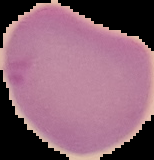
result: malaria parasites identified
preparation: thin blood film
image_type: segmented cell region on a black background
image_size: 154×160 pixels